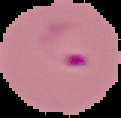
malaria status = parasitized
image size = 121×118 pixels
image type = segmented cell region with the area outside set to black
preparation = thin blood smear